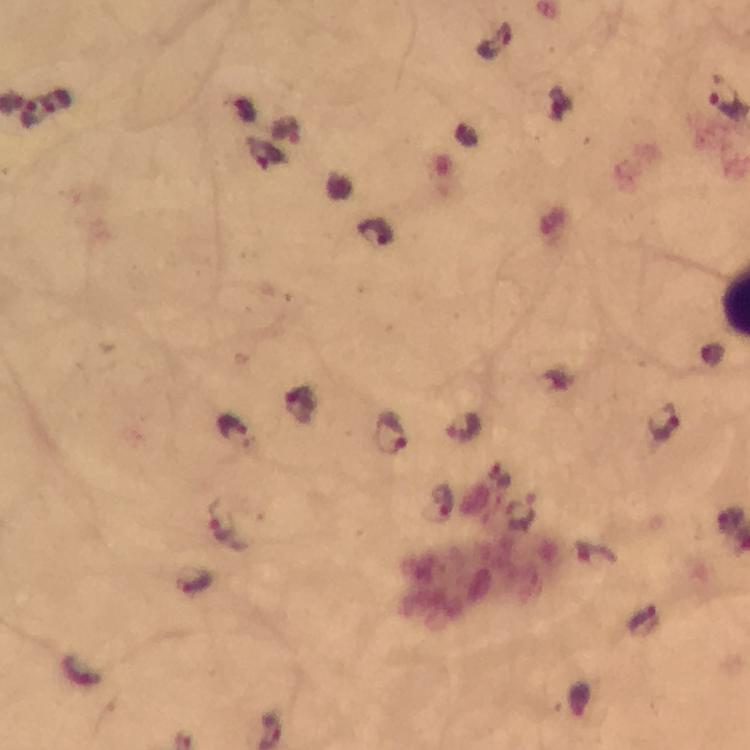

Approximate centers as {x, y} in pixels.
Summary:
  - Plasmodium parasite locations: {494, 39}, {729, 97}, {56, 101}, {32, 112}, {285, 128}, {376, 233}, {299, 404}, {664, 422}, {462, 425}, {233, 428}, {394, 430}, {444, 500}, {223, 523}, {192, 580}, {643, 621}
  - Cropped from: a single field of view
  - Preparation: thick smear
  - Capture: smartphone camera through the microscope
  - Stain: Giemsa
  - Immersion oil: used
  - Context: from a diagnostic examination for malaria
  - Magnification: 100x
  - Image size: 750×750 pixels